Classify this cell by malaria status.
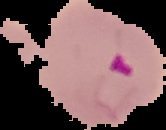
It is parasitized.

image type = cell region segmented out of the field of view; surrounding area masked to black
preparation = thin blood film
image size = 166×130 pixels